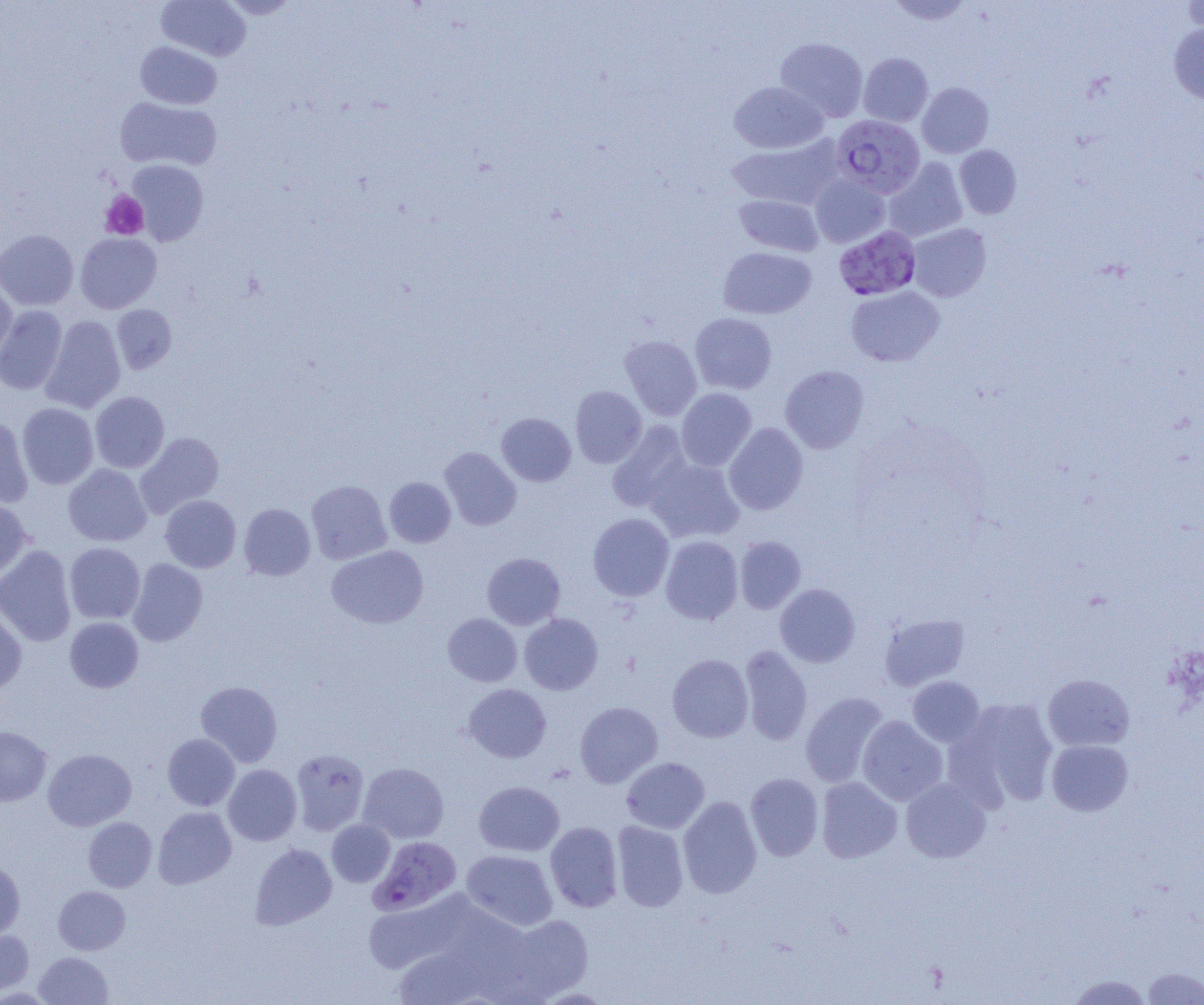
Summary:
  - Coordinate format: approximate bounding boxes as named x1/y1/x2/y2 corners in pixels
  - Platelet locations: (x1=100, y1=190, x2=149, y2=240)
  - Uninfected red blood cell locations: (x1=156, y1=0, x2=251, y2=61), (x1=220, y1=0, x2=300, y2=19), (x1=887, y1=0, x2=975, y2=25), (x1=1182, y1=0, x2=1204, y2=37), (x1=1168, y1=23, x2=1204, y2=104), (x1=775, y1=37, x2=868, y2=122), (x1=135, y1=41, x2=222, y2=109), (x1=858, y1=52, x2=933, y2=127), (x1=729, y1=81, x2=828, y2=154), (x1=917, y1=82, x2=994, y2=158), (x1=115, y1=96, x2=221, y2=171), (x1=726, y1=135, x2=842, y2=210), (x1=954, y1=145, x2=1021, y2=219), (x1=884, y1=158, x2=967, y2=242), (x1=127, y1=160, x2=209, y2=245), (x1=810, y1=174, x2=890, y2=248), (x1=734, y1=194, x2=823, y2=256), (x1=907, y1=223, x2=991, y2=302), (x1=0, y1=229, x2=79, y2=311), (x1=75, y1=232, x2=161, y2=314), (x1=718, y1=247, x2=816, y2=319), (x1=0, y1=280, x2=18, y2=367), (x1=846, y1=286, x2=944, y2=367), (x1=111, y1=304, x2=177, y2=374), (x1=0, y1=305, x2=67, y2=395), (x1=690, y1=313, x2=777, y2=394), (x1=40, y1=316, x2=126, y2=414), (x1=620, y1=335, x2=702, y2=420), (x1=780, y1=365, x2=869, y2=453), (x1=570, y1=386, x2=647, y2=468), (x1=676, y1=388, x2=756, y2=471), (x1=90, y1=391, x2=170, y2=473), (x1=17, y1=403, x2=99, y2=489), (x1=496, y1=413, x2=576, y2=486), (x1=0, y1=414, x2=33, y2=508), (x1=607, y1=421, x2=692, y2=512), (x1=724, y1=422, x2=808, y2=515), (x1=135, y1=432, x2=224, y2=518), (x1=439, y1=447, x2=521, y2=531), (x1=644, y1=457, x2=744, y2=543), (x1=63, y1=464, x2=152, y2=546), (x1=384, y1=477, x2=456, y2=547), (x1=306, y1=480, x2=392, y2=565), (x1=160, y1=495, x2=241, y2=573), (x1=0, y1=497, x2=31, y2=582), (x1=238, y1=503, x2=316, y2=581), (x1=588, y1=513, x2=674, y2=601), (x1=660, y1=536, x2=743, y2=624), (x1=735, y1=536, x2=806, y2=613), (x1=64, y1=542, x2=145, y2=624), (x1=0, y1=545, x2=76, y2=647), (x1=326, y1=545, x2=429, y2=629), (x1=482, y1=552, x2=565, y2=630), (x1=127, y1=559, x2=208, y2=647), (x1=775, y1=584, x2=860, y2=667), (x1=0, y1=606, x2=27, y2=696), (x1=443, y1=613, x2=522, y2=687), (x1=519, y1=613, x2=603, y2=694), (x1=880, y1=613, x2=970, y2=691), (x1=65, y1=617, x2=144, y2=693), (x1=739, y1=645, x2=812, y2=746), (x1=667, y1=654, x2=753, y2=742), (x1=1042, y1=674, x2=1135, y2=752), (x1=907, y1=676, x2=985, y2=747), (x1=195, y1=680, x2=283, y2=767), (x1=463, y1=683, x2=551, y2=762), (x1=800, y1=692, x2=889, y2=788), (x1=948, y1=696, x2=1060, y2=809), (x1=575, y1=701, x2=663, y2=788), (x1=857, y1=716, x2=947, y2=806), (x1=0, y1=726, x2=51, y2=806), (x1=162, y1=733, x2=240, y2=810), (x1=1046, y1=739, x2=1133, y2=816), (x1=42, y1=749, x2=136, y2=831), (x1=290, y1=749, x2=369, y2=835), (x1=621, y1=757, x2=709, y2=834), (x1=358, y1=762, x2=449, y2=843), (x1=223, y1=764, x2=301, y2=845), (x1=745, y1=772, x2=824, y2=861), (x1=816, y1=777, x2=902, y2=863), (x1=901, y1=777, x2=991, y2=863), (x1=474, y1=781, x2=565, y2=857), (x1=678, y1=795, x2=762, y2=898), (x1=152, y1=806, x2=236, y2=889), (x1=83, y1=817, x2=157, y2=892), (x1=327, y1=819, x2=395, y2=887), (x1=612, y1=820, x2=688, y2=912), (x1=545, y1=821, x2=623, y2=912), (x1=250, y1=843, x2=337, y2=930), (x1=461, y1=849, x2=558, y2=931), (x1=0, y1=860, x2=25, y2=941), (x1=53, y1=886, x2=130, y2=955), (x1=361, y1=889, x2=487, y2=975), (x1=500, y1=913, x2=593, y2=1001), (x1=0, y1=930, x2=34, y2=996), (x1=390, y1=942, x2=499, y2=1005), (x1=34, y1=951, x2=112, y2=1005), (x1=1142, y1=967, x2=1204, y2=1004), (x1=1065, y1=974, x2=1154, y2=1004)
  - Plasmodium falciparum-infected red blood cell locations: (x1=832, y1=114, x2=925, y2=197), (x1=834, y1=225, x2=921, y2=301), (x1=370, y1=835, x2=462, y2=915)
  - Slide-level diagnosis: Plasmodium falciparum
  - Magnification: 1000x
  - Preparation: thin blood film
  - Modality: optical microscopy
  - Field of view: one of a larger specimen
  - Image size: 1204×1005 pixels